Find each parasitized RBC.
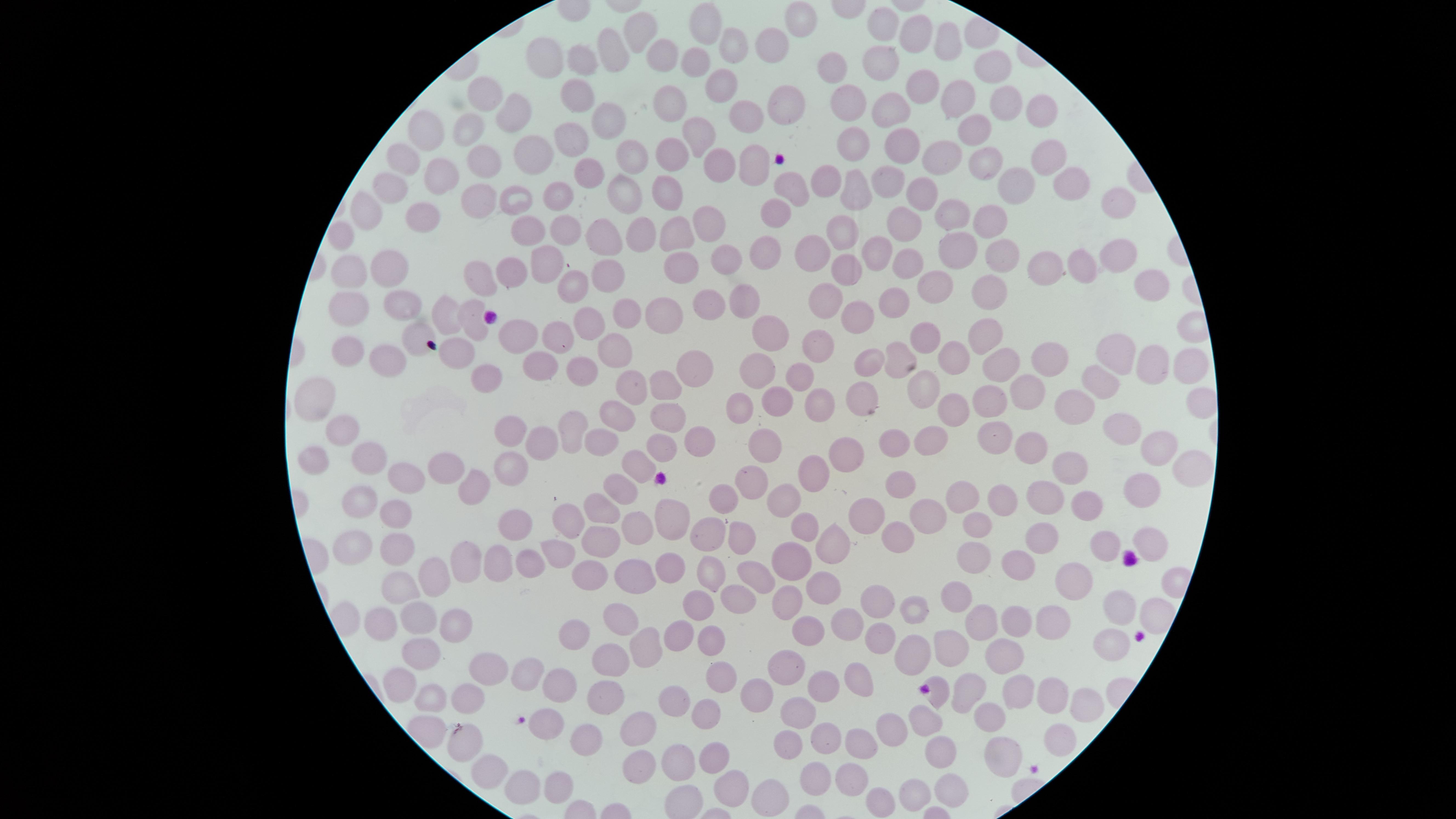
No parasitized RBCs identified.

capture: smartphone photograph through the microscope eyepiece
image_size: 1456×819 pixels
uninfected_RBCs: 'approximate marker points as {x, y} in pixels: {799, 18}, {888, 23}, {703, 24}, {637, 31}, {912, 33}, {951, 42}, {776, 44}, {732, 46}, {616, 51}, {879, 53}, {660, 54}, {547, 55}, {585, 59}, {689, 63}, {988, 65}, {834, 70}, {717, 86}, {917, 89}, {675, 94}, {582, 96}, {488, 99}, {952, 100}, {885, 101}, {1003, 103}, {788, 104}, {847, 104}, {1034, 110}, {518, 116}, {608, 116}, {745, 117}, {424, 128}, {984, 129}, {468, 130}, {575, 133}, {691, 136}, {528, 144}, {856, 144}, {900, 146}, {675, 153}, {628, 155}, {1041, 156}, {483, 157}, {944, 157}, {402, 160}, {754, 163}, {713, 169}, {982, 170}, {586, 173}, {439, 176}, {889, 177}, {816, 180}, {1068, 182}, {851, 183}, {1018, 185}, {672, 188}, {789, 188}, {393, 190}, {562, 193}, {622, 193}, {922, 195}, {512, 197}, {478, 200}, {1118, 202}, {774, 207}, {369, 211}, {951, 211}, {422, 216}, {990, 216}, {715, 220}, {900, 224}, {679, 225}, {530, 226}, {639, 226}, {565, 229}, {606, 234}, {343, 235}, {838, 236}, {964, 245}, {885, 248}, {1007, 250}, {762, 251}, {814, 253}, {1112, 253}, {729, 259}, {908, 259}, {547, 263}, {1080, 263}, {386, 265}, {848, 266}, {511, 267}, {679, 267}, {1055, 267}, {609, 268}, {349, 272}, {928, 279}, {1145, 279}, {485, 282}, {988, 287}, {571, 288}, {747, 298}, {895, 298}, {820, 299}, {399, 304}, {710, 304}, {452, 311}, {616, 312}, {865, 313}, {356, 314}, {469, 315}, {659, 315}, {587, 324}, {418, 330}, {771, 333}, {988, 333}, {557, 335}, {515, 337}, {931, 340}, {621, 342}, {817, 345}, {347, 347}, {459, 348}, {1120, 348}, {900, 352}, {1050, 356}, {953, 357}, {875, 359}, {388, 360}, {1186, 360}, {689, 361}, {1155, 362}, {583, 365}, {1001, 366}, {542, 368}, {755, 370}, {796, 370}, {491, 374}, {1104, 381}, {634, 383}, {664, 385}, {925, 389}, {866, 390}, {1033, 390}, {316, 393}, {817, 393}, {986, 395}, {1200, 398}, {777, 399}, {1070, 402}, {743, 407}, {955, 407}, {670, 409}, {616, 410}, {344, 424}, {573, 426}, {1122, 426}, {992, 432}, {509, 434}, {660, 439}, {698, 439}, {545, 441}, {595, 442}, {769, 442}, {894, 443}, {1034, 443}, {1159, 444}, {929, 446}, {849, 452}, {371, 457}, {1179, 459}, {317, 460}, {634, 464}, {508, 466}, {443, 468}, {811, 469}, {1073, 469}, {478, 477}, {404, 478}, {745, 478}, {904, 478}, {621, 484}, {1145, 486}, {1041, 493}, {962, 495}, {362, 496}, {787, 498}, {994, 498}, {725, 502}, {867, 504}, {600, 505}, {1087, 510}, {393, 515}, {667, 516}, {923, 518}, {516, 522}, {972, 522}, {566, 523}, {631, 526}, {800, 526}, {892, 529}, {601, 532}, {741, 535}, {1051, 535}, {709, 536}, {347, 543}, {387, 544}, {1106, 544}, {1141, 544}, {825, 545}, {553, 555}, {971, 557}, {1019, 557}, {464, 561}, {492, 561}, {789, 562}, {523, 564}, {664, 564}, {711, 569}, {590, 571}, {632, 578}, {750, 578}, {438, 579}, {404, 582}, {1078, 583}, {821, 586}, {960, 590}, {737, 598}, {699, 600}, {786, 600}, {883, 601}, {1119, 606}, {917, 608}, {624, 613}, {1011, 615}, {985, 616}, {451, 619}, {416, 620}, {375, 621}, {840, 621}, {1054, 622}, {710, 632}, {579, 633}, {880, 634}, {667, 635}, {799, 635}, {947, 644}, {1108, 645}, {635, 646}, {913, 650}, {416, 652}, {997, 652}, {607, 660}, {792, 664}, {496, 670}, {525, 673}, {716, 673}, {859, 673}, {403, 678}, {566, 681}, {823, 684}, {972, 685}, {1013, 690}, {1044, 690}, {604, 691}, {761, 692}, {939, 693}, {424, 695}, {463, 698}, {676, 701}, {1085, 701}, {799, 709}, {989, 715}, {703, 717}, {926, 721}, {641, 724}, {545, 729}, {899, 730}, {581, 732}, {821, 734}, {463, 736}, {863, 739}, {999, 747}, {939, 748}, {790, 749}, {716, 752}, {683, 757}, {642, 762}, {485, 764}, {849, 772}, {812, 777}, {556, 781}, {732, 782}, {948, 782}, {521, 787}, {913, 791}, {770, 793}, {883, 798}'
field_of_view: single
preparation: thin smear of blood
visible_region: circular
stain: Giemsa